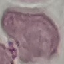
Malaria status: uninfected. Acquired by smartphone through the microscope eyepiece. Thin blood smear. Automatically extracted cell patch, resized to 64 × 64 pixels. Giemsa stain.